Name the cell type shown.
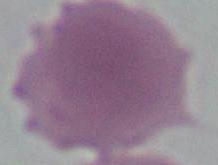

This is an erythrocyte.

magnification = 1000x
modality = micrograph